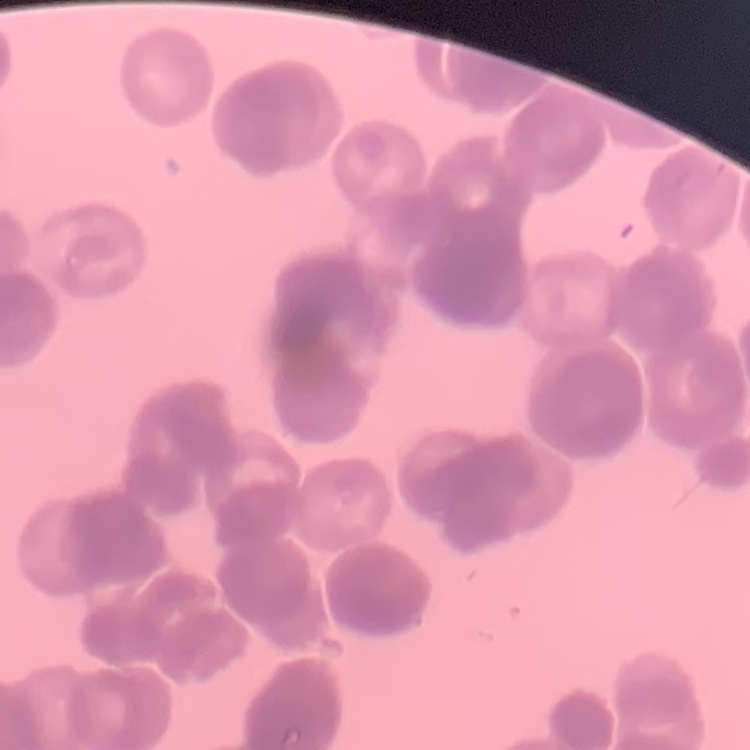 The erythrocytes exhibit rouleaux formation. Square crop of a larger photomicrograph. Thin peripheral smear. Field's or Giemsa stain.